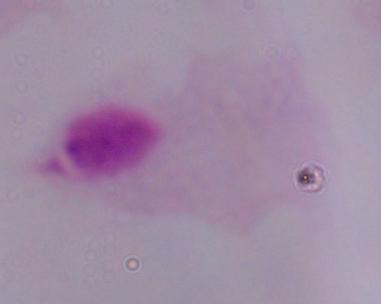

Summary:
  - Magnification: 1000x
  - Identification: trichomonad
  - Modality: micrograph